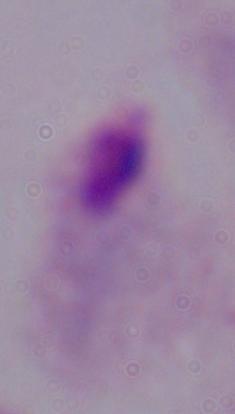
magnification = 1000x
modality = photomicrograph
identification = trichomonad